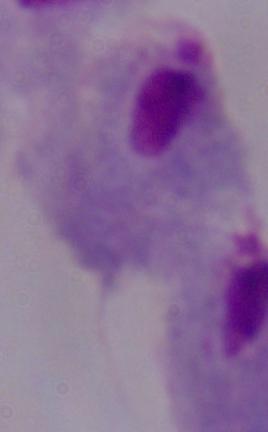
{
  "modality": "photomicrograph",
  "identification": "trichomonad",
  "magnification": "1000x"
}